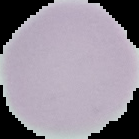
image_type: cell region segmented out of the field of view; surrounding area masked to black
malaria_status: uninfected
image_size: 139×139 pixels
preparation: thin blood film